Report the malaria status.
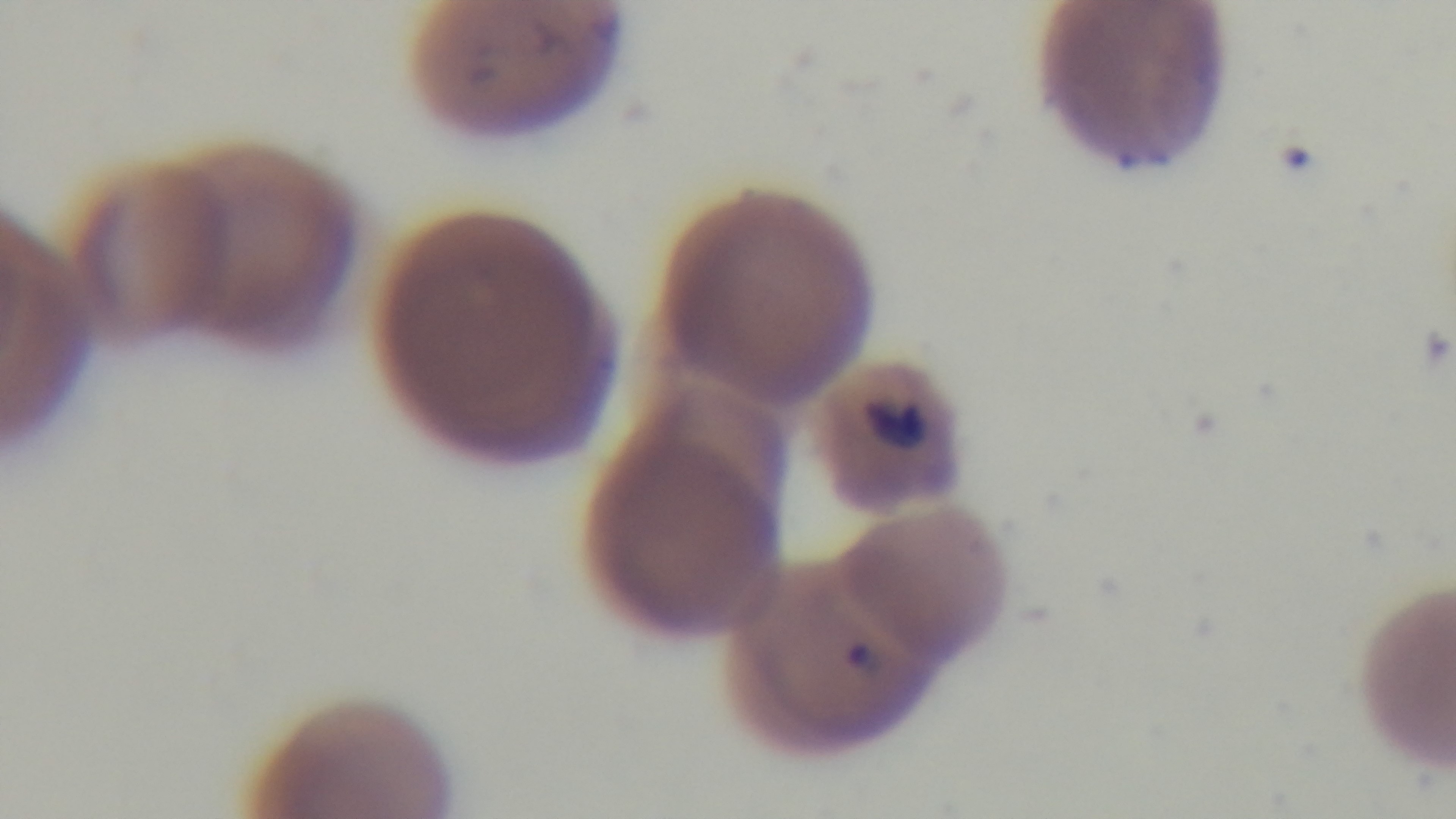

Infected.

{
  "stain": "Giemsa",
  "objective": "100x oil immersion",
  "field_of_view": "one from the slide",
  "modality": "light microscopy",
  "capture": "mounted 4K digital camera",
  "preparation": "thin smear"
}